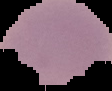

Summary:
  - Image type: segmented cell region with the area outside set to black
  - Malaria status: uninfected
  - Image size: 112×91 pixels
  - Preparation: thin blood film